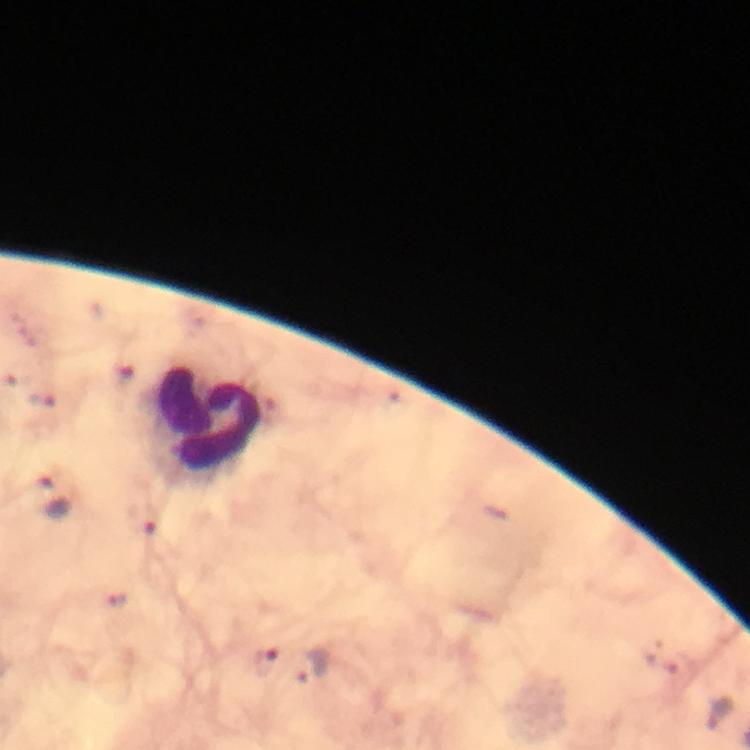

Approximate centers as {x, y} in pixels. Leukocyte locations: {208, 421}. Malaria parasite locations: {54, 497}, {149, 522}, {267, 661}, {313, 666}, {721, 713}. Cropped region of a single field of view. From a malaria diagnostic workup. 100x magnification. Thick blood film. Photographed through the microscope with a smartphone camera. Immersion oil applied. Giemsa-stained preparation. Image is 750×750 pixels.